Assess this cell for malaria.
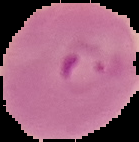
It is parasitized.

Summary:
  - Image size: 139×142 pixels
  - Image type: segmented cell region with the area outside set to black
  - Preparation: thin blood film